State which cell type is depicted.
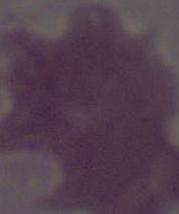

An erythrocyte.

Summary:
  - Magnification: 1000x
  - Modality: micrograph